Name the blood parasite species.
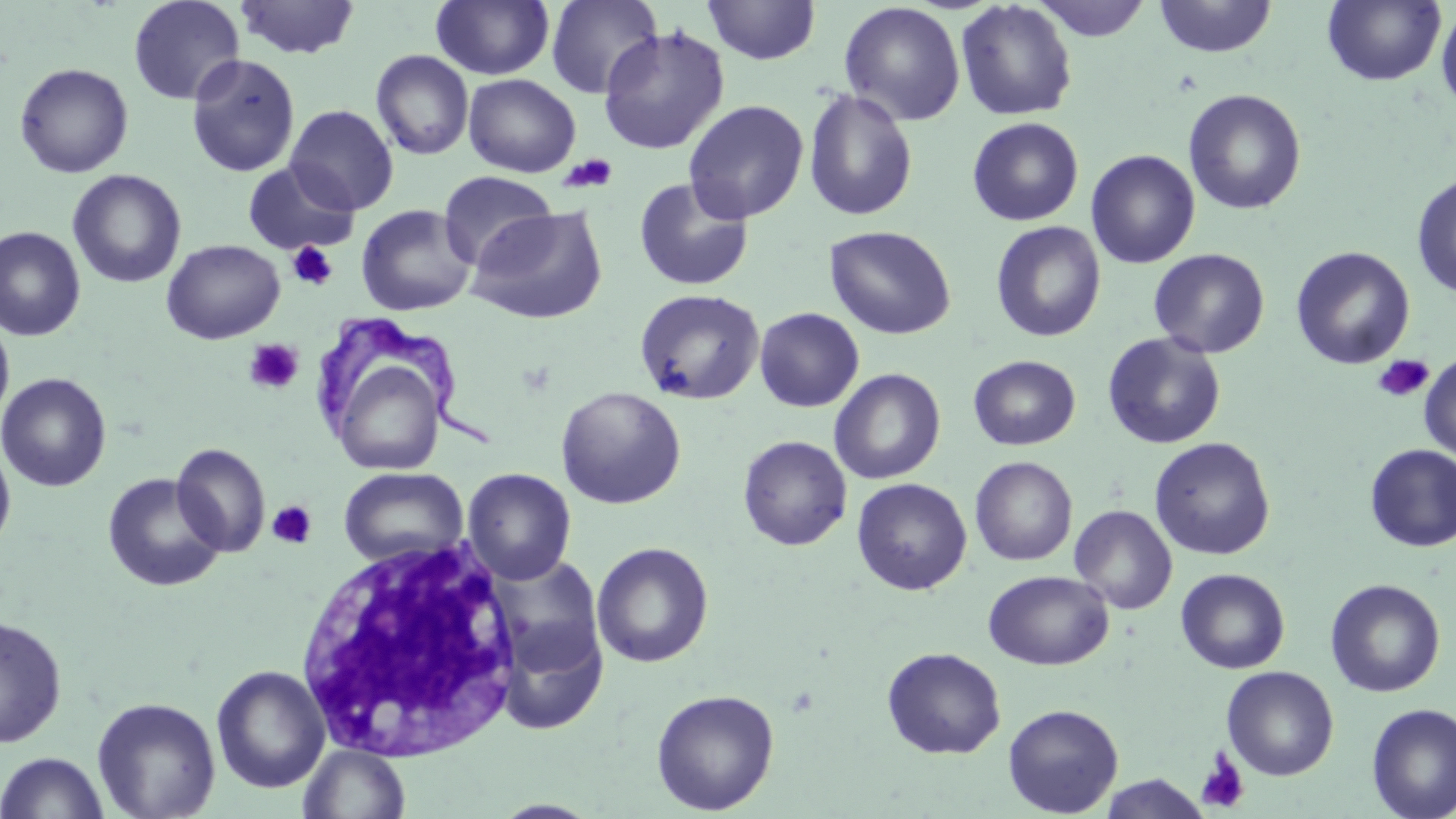

Trypanosoma brucei.

Approximate bounding boxes as named x1/y1/x2/y2 corners in pixels. Trypanosoma brucei locations: (x1=318, y1=312, x2=503, y2=455). Uninfected red blood cell locations: (x1=127, y1=0, x2=245, y2=105), (x1=234, y1=0, x2=360, y2=59), (x1=431, y1=0, x2=555, y2=80), (x1=545, y1=0, x2=663, y2=99), (x1=1031, y1=0, x2=1152, y2=41), (x1=1154, y1=0, x2=1277, y2=59), (x1=1322, y1=0, x2=1447, y2=86), (x1=703, y1=1, x2=821, y2=65), (x1=955, y1=1, x2=1077, y2=121), (x1=839, y1=2, x2=966, y2=126), (x1=1436, y1=4, x2=1456, y2=115), (x1=597, y1=25, x2=730, y2=155), (x1=370, y1=49, x2=474, y2=160), (x1=186, y1=53, x2=300, y2=177), (x1=14, y1=62, x2=134, y2=178), (x1=463, y1=74, x2=581, y2=177), (x1=803, y1=86, x2=919, y2=222), (x1=1183, y1=89, x2=1307, y2=215), (x1=683, y1=100, x2=808, y2=224), (x1=285, y1=104, x2=399, y2=215), (x1=967, y1=117, x2=1084, y2=226), (x1=1086, y1=149, x2=1200, y2=268), (x1=243, y1=162, x2=359, y2=255), (x1=67, y1=169, x2=187, y2=288), (x1=438, y1=171, x2=558, y2=271), (x1=1411, y1=173, x2=1456, y2=301), (x1=633, y1=177, x2=755, y2=292), (x1=356, y1=204, x2=477, y2=316), (x1=466, y1=206, x2=608, y2=325), (x1=990, y1=221, x2=1106, y2=342), (x1=0, y1=226, x2=86, y2=341), (x1=825, y1=226, x2=956, y2=340), (x1=161, y1=239, x2=285, y2=344), (x1=1290, y1=246, x2=1415, y2=370), (x1=1148, y1=248, x2=1270, y2=359), (x1=634, y1=288, x2=764, y2=405), (x1=754, y1=307, x2=864, y2=412), (x1=0, y1=313, x2=15, y2=428), (x1=1102, y1=332, x2=1226, y2=449), (x1=1419, y1=353, x2=1456, y2=462), (x1=969, y1=355, x2=1081, y2=450), (x1=335, y1=363, x2=437, y2=477), (x1=829, y1=369, x2=946, y2=484), (x1=0, y1=372, x2=112, y2=492), (x1=555, y1=386, x2=686, y2=509), (x1=737, y1=435, x2=852, y2=551), (x1=1150, y1=437, x2=1275, y2=560), (x1=0, y1=439, x2=16, y2=556), (x1=172, y1=443, x2=271, y2=557), (x1=1364, y1=445, x2=1456, y2=552), (x1=970, y1=456, x2=1078, y2=566), (x1=338, y1=467, x2=468, y2=568), (x1=462, y1=468, x2=577, y2=585), (x1=102, y1=472, x2=227, y2=593), (x1=852, y1=478, x2=972, y2=595), (x1=1070, y1=505, x2=1177, y2=614), (x1=591, y1=542, x2=714, y2=668), (x1=487, y1=555, x2=607, y2=684), (x1=1176, y1=568, x2=1290, y2=674), (x1=983, y1=570, x2=1114, y2=670), (x1=1325, y1=578, x2=1446, y2=697), (x1=0, y1=614, x2=67, y2=748), (x1=496, y1=618, x2=608, y2=736), (x1=882, y1=647, x2=1006, y2=759), (x1=211, y1=665, x2=330, y2=794), (x1=1222, y1=666, x2=1338, y2=781), (x1=651, y1=688, x2=780, y2=815), (x1=91, y1=697, x2=221, y2=818), (x1=1003, y1=703, x2=1124, y2=817), (x1=1367, y1=703, x2=1456, y2=819), (x1=299, y1=744, x2=410, y2=819), (x1=0, y1=751, x2=109, y2=818), (x1=1099, y1=774, x2=1210, y2=818). Platelet locations: (x1=558, y1=154, x2=619, y2=193), (x1=287, y1=241, x2=338, y2=291), (x1=244, y1=339, x2=304, y2=394), (x1=1372, y1=354, x2=1434, y2=403), (x1=267, y1=501, x2=317, y2=549), (x1=1196, y1=749, x2=1250, y2=814). White blood cell locations: (x1=294, y1=536, x2=526, y2=764). Image is 1456×819 pixels. May-Grünwald-Giemsa-stained preparation. Single field of view. Thin blood smear. Captured at 1000x magnification. Optical microscopy.